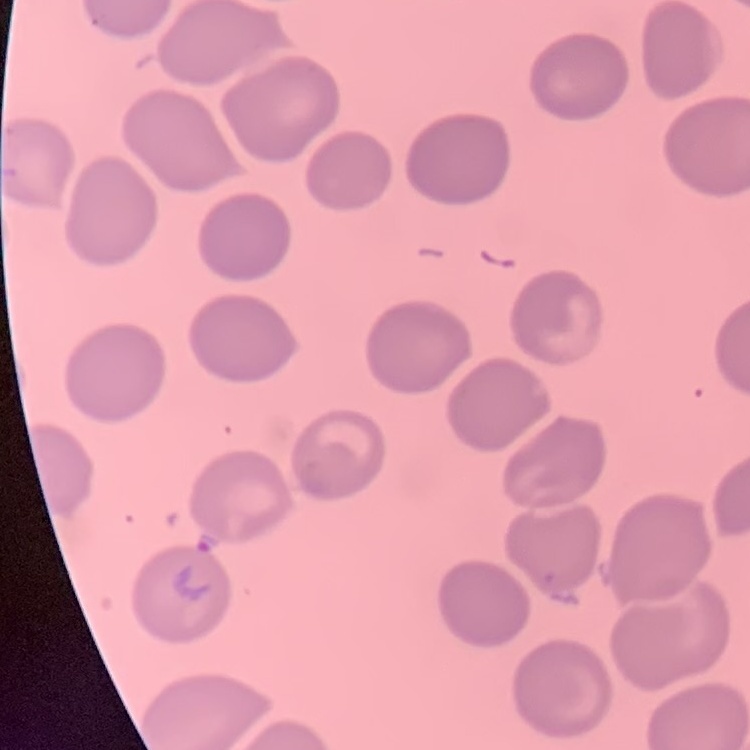 The erythrocytes exhibit no rouleaux formation. Field's or Giemsa stain. Thin blood smear. One tile cut from a larger photomicrograph.